Assess this cell for malaria.
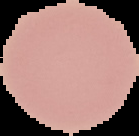
It is uninfected.

Summary:
  - Image type: segmented cell region with the area outside set to black
  - Preparation: thin blood film
  - Image size: 139×136 pixels